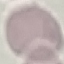

result = no malaria parasites detected
stain = Giemsa
capture = smartphone camera at the microscope eyepiece
preparation = thin blood film
image type = automatically extracted cell patch, resized to 64 × 64 pixels